Name the cell type shown.
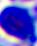
This is a leukocyte.

Captured at 400x magnification. Micrograph.